Locate and identify every blood parasite.
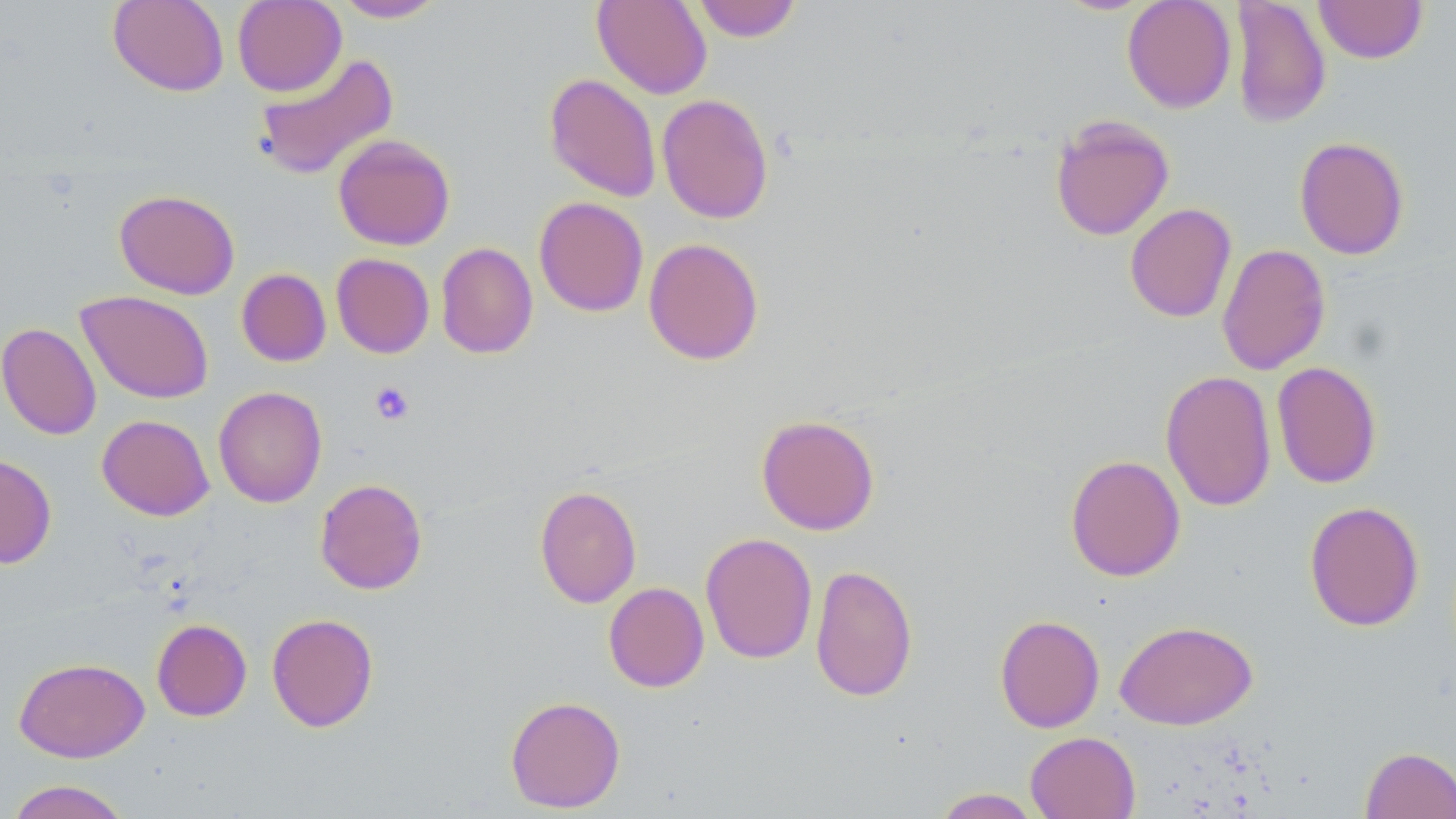

No blood parasites seen.

Approximate bounding boxes as [x1, y1, x2, y2] in pixels. Uninfected red blood cell locations: [108, 0, 229, 96], [232, 0, 347, 97], [333, 0, 446, 22], [592, 0, 712, 99], [692, 0, 802, 42], [1122, 0, 1236, 113], [1229, 0, 1331, 129], [1314, 0, 1427, 63], [252, 52, 399, 182], [544, 73, 662, 202], [657, 93, 774, 224], [1050, 115, 1175, 241], [333, 134, 456, 250], [1294, 136, 1409, 260], [114, 189, 240, 299], [534, 196, 649, 317], [1125, 203, 1237, 323], [643, 237, 764, 365], [436, 242, 538, 359], [1216, 243, 1331, 375], [331, 253, 434, 358], [236, 268, 331, 367], [76, 290, 214, 404], [0, 322, 102, 440], [1271, 361, 1382, 489], [1160, 370, 1277, 512], [213, 386, 327, 508], [97, 414, 214, 521], [756, 414, 880, 535], [0, 453, 57, 569], [1064, 454, 1186, 582], [314, 478, 428, 595], [534, 484, 642, 608], [1304, 501, 1425, 632], [700, 532, 817, 664], [810, 564, 918, 702], [603, 582, 709, 692], [266, 613, 379, 732], [995, 614, 1105, 733], [152, 618, 252, 721], [1115, 620, 1258, 730], [13, 657, 149, 763], [505, 695, 625, 813], [1025, 731, 1141, 819], [1360, 745, 1456, 819], [4, 779, 133, 819], [931, 787, 1041, 818]. Platelet locations: [369, 382, 415, 425]. Slide-level diagnosis: no evidence of blood parasites. Thin blood film. May-Grünwald-Giemsa stain. Light microscopy. Image is 1456×819 pixels. Single field of view. 1000x magnification.